State which parasite is depicted.
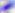

This is Toxoplasma gondii.

Summary:
  - Magnification: 400x
  - Modality: micrograph